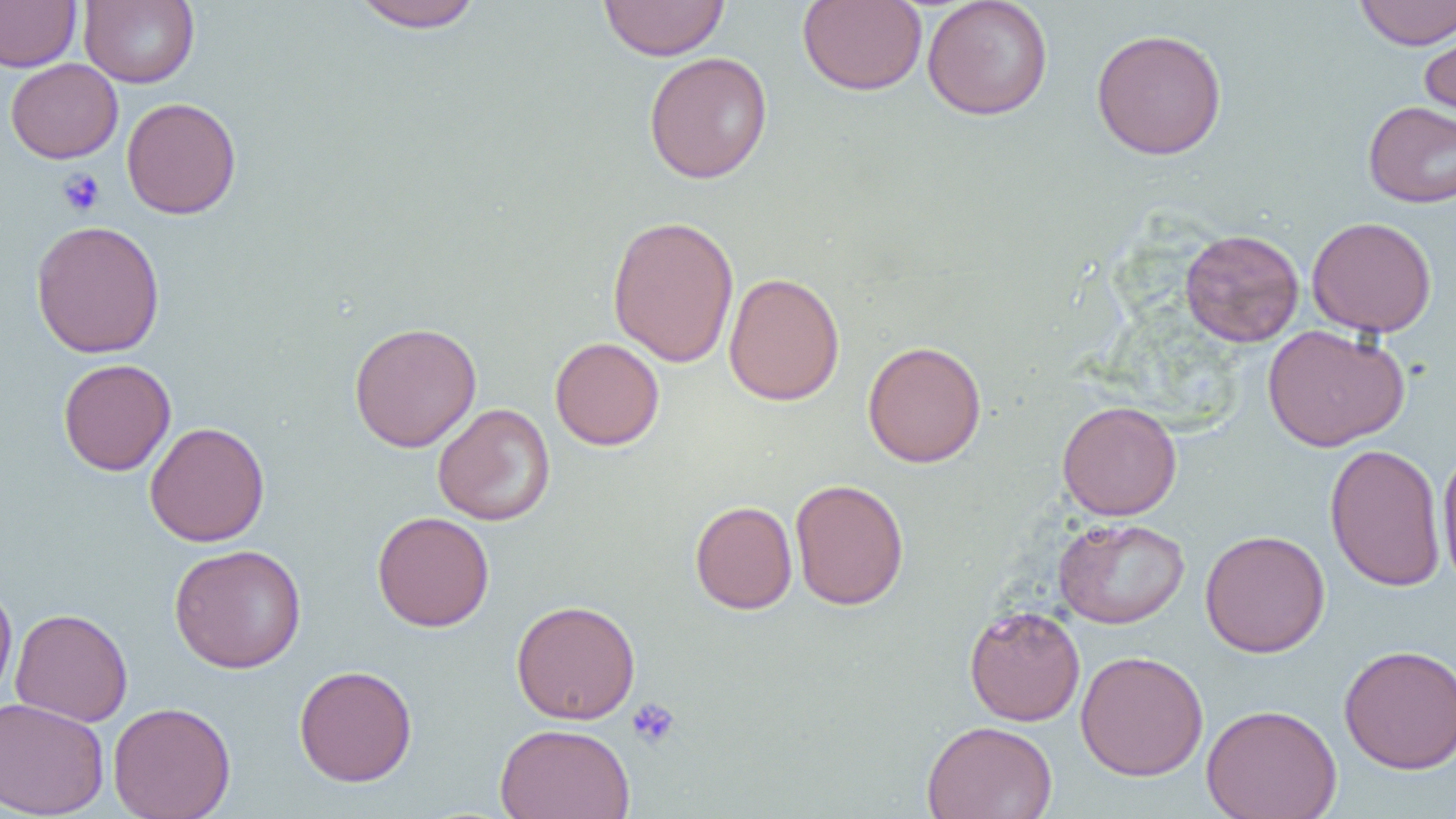

Approximate bounding boxes as [x1, y1, x2, y2] in pixels. Platelet locations: [57, 168, 105, 216], [627, 697, 681, 750]. Uninfected red blood cell locations: [0, 0, 81, 72], [79, 0, 200, 88], [349, 0, 485, 32], [598, 0, 730, 61], [797, 0, 927, 96], [922, 0, 1053, 121], [1354, 0, 1456, 50], [1419, 16, 1456, 127], [1090, 27, 1228, 160], [643, 51, 773, 183], [5, 58, 123, 163], [121, 97, 241, 219], [1362, 100, 1456, 208], [607, 214, 740, 368], [1306, 216, 1437, 338], [29, 219, 166, 358], [1179, 228, 1305, 347], [723, 272, 846, 406], [348, 321, 482, 453], [1262, 324, 1410, 452], [550, 337, 665, 451], [862, 340, 987, 468], [58, 358, 176, 476], [1056, 400, 1182, 520], [432, 403, 555, 526], [144, 421, 271, 547], [1324, 443, 1447, 592], [1437, 446, 1456, 590], [789, 478, 909, 610], [690, 500, 798, 615], [372, 512, 495, 632], [1053, 516, 1190, 629], [1199, 529, 1330, 657], [169, 543, 308, 674], [0, 580, 18, 707], [511, 599, 641, 724], [963, 605, 1086, 726], [10, 608, 133, 726], [1338, 643, 1456, 774], [1075, 650, 1209, 781], [293, 664, 417, 787], [0, 697, 110, 818], [107, 701, 236, 819], [1201, 703, 1342, 819], [921, 720, 1058, 819], [494, 723, 635, 819]. Slide-level diagnosis: negative for blood parasites. Image is 1456×819 pixels. Thin blood smear. 1000x magnification. One field of a larger specimen. Optical microscopy.